Name the blood parasite species.
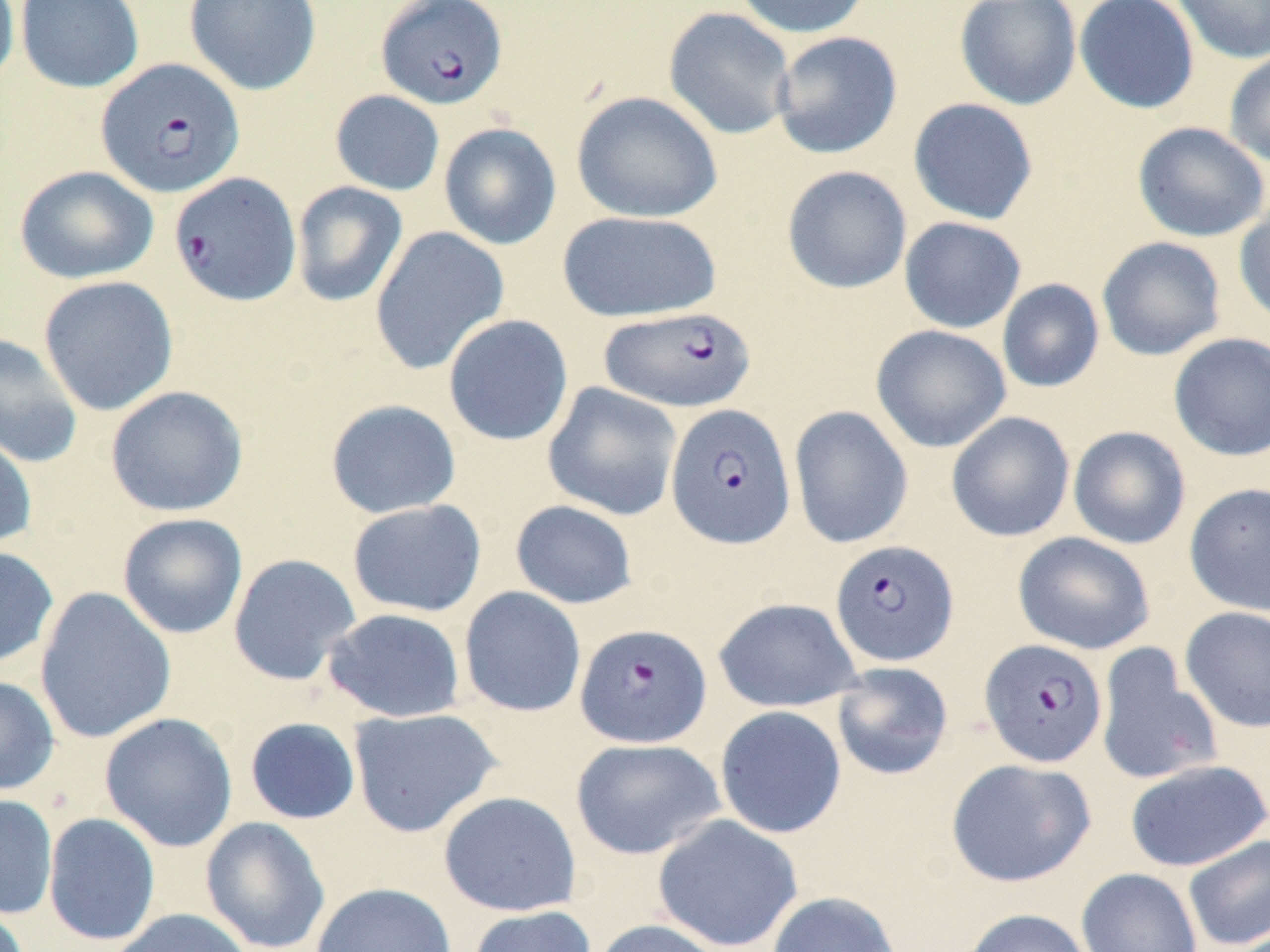

Plasmodium falciparum.

Approximate bounding boxes as [x1, y1, x2, y2] in pixels. Plasmodium falciparum-infected red blood cell locations: [376, 0, 507, 110], [95, 58, 244, 199], [169, 171, 302, 307], [598, 305, 756, 412], [666, 403, 796, 550], [830, 540, 958, 666], [575, 622, 712, 748], [979, 638, 1107, 768]. Uninfected red blood cell locations: [0, 0, 20, 89], [15, 0, 144, 93], [184, 0, 321, 96], [732, 0, 872, 39], [955, 0, 1082, 110], [1074, 0, 1199, 114], [1170, 0, 1270, 64], [663, 7, 797, 140], [771, 31, 903, 159], [1224, 48, 1270, 170], [330, 90, 445, 196], [571, 91, 723, 223], [908, 97, 1039, 225], [1132, 121, 1269, 242], [438, 122, 561, 250], [14, 165, 159, 284], [781, 165, 912, 294], [290, 181, 408, 308], [1234, 198, 1270, 328], [556, 210, 722, 322], [899, 217, 1027, 334], [370, 226, 509, 375], [1097, 236, 1227, 361], [37, 275, 178, 416], [997, 278, 1105, 393], [442, 314, 574, 447], [871, 325, 1012, 453], [0, 332, 83, 469], [1168, 332, 1270, 462], [542, 381, 683, 521], [105, 385, 250, 517], [325, 398, 462, 519], [789, 405, 913, 549], [946, 411, 1075, 542], [1068, 425, 1191, 549], [0, 426, 38, 550], [1184, 483, 1270, 616], [346, 499, 486, 618], [510, 499, 639, 609], [117, 512, 248, 639], [1012, 531, 1155, 655], [0, 545, 59, 670], [228, 553, 362, 686], [34, 586, 176, 744], [458, 586, 586, 718], [713, 597, 863, 712], [1179, 605, 1270, 733], [321, 607, 467, 723], [1095, 644, 1222, 786], [831, 661, 954, 781], [0, 674, 60, 796], [714, 705, 847, 839], [348, 707, 502, 838], [99, 712, 238, 852], [244, 717, 361, 825], [570, 737, 725, 860], [945, 757, 1095, 888], [1124, 759, 1269, 872], [438, 791, 582, 917], [0, 794, 58, 919], [43, 812, 161, 946], [652, 814, 803, 952], [200, 816, 331, 952], [1183, 834, 1270, 951], [1076, 867, 1202, 952], [311, 882, 457, 952], [766, 891, 902, 952], [467, 905, 597, 952], [107, 908, 256, 952], [959, 908, 1092, 952], [591, 919, 728, 952]. May-Grünwald-Giemsa-stained preparation. Thin blood smear. Optical microscopy. Single field of view. Image is 1270×952 pixels. Captured at 1000x magnification.